Describe the morphology of the erythrocytes.
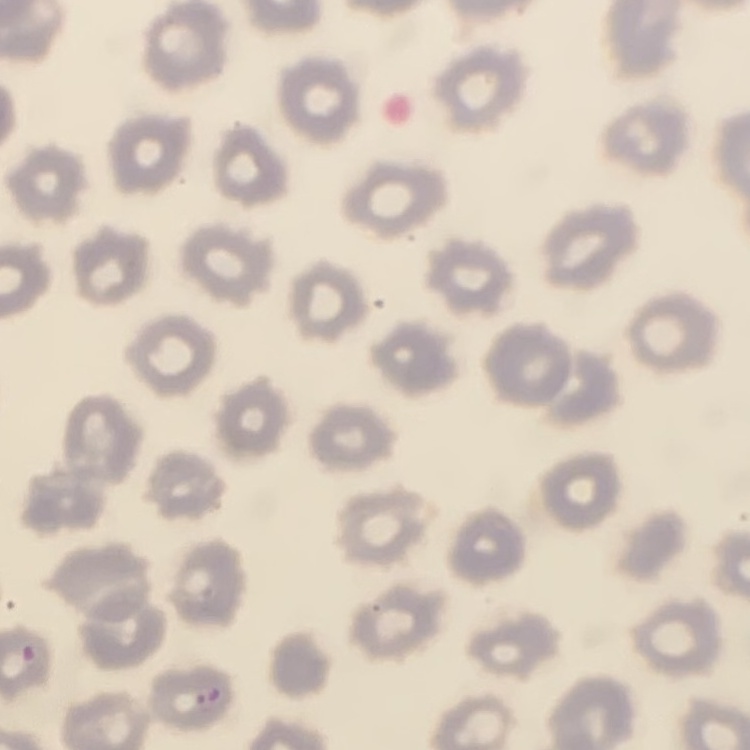
They show no rouleaux formation.

preparation = thin blood film
image type = square crop of a larger photomicrograph
stain = Field's or Giemsa